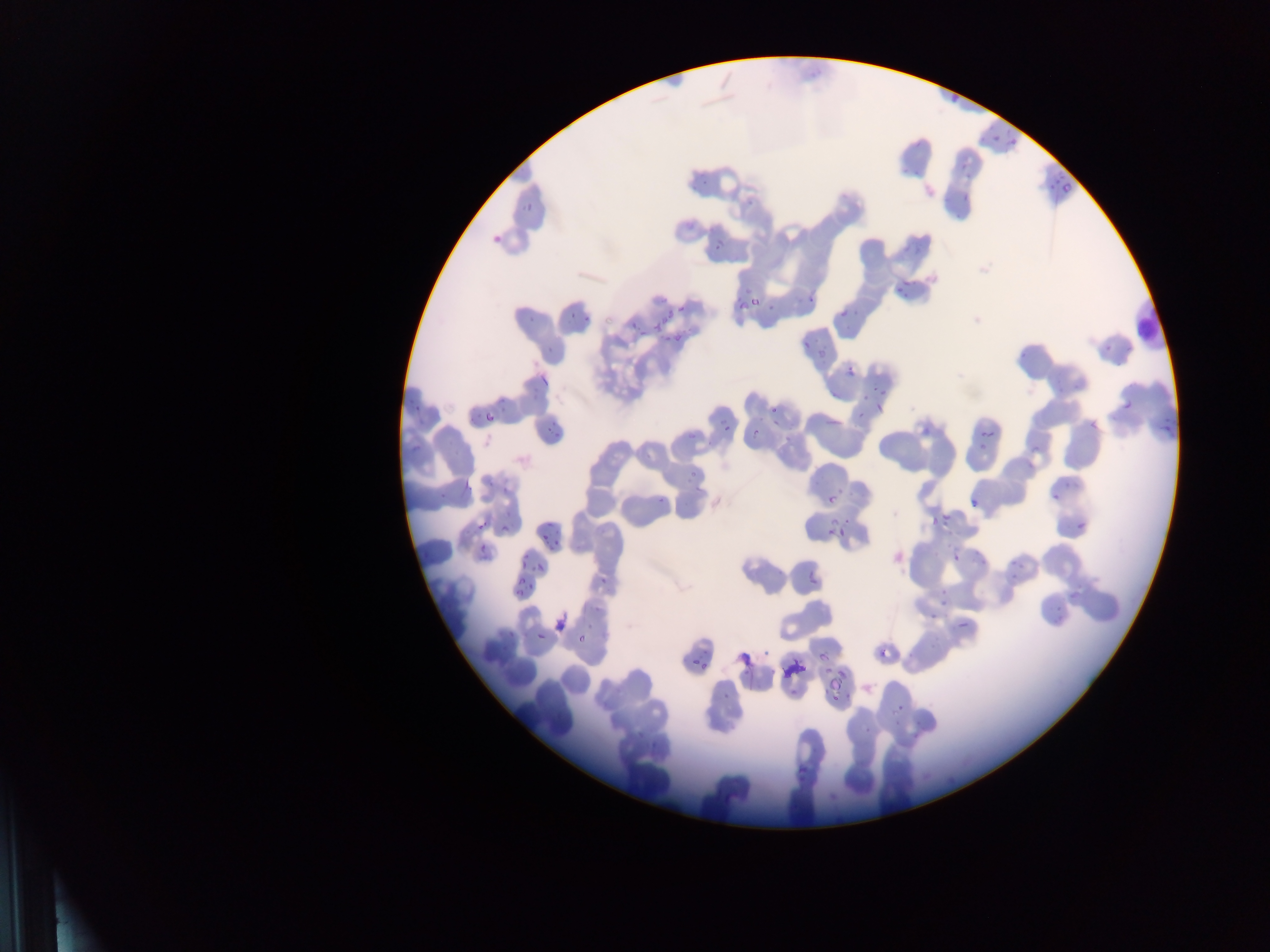
Approximate bounding boxes as (left, top, right, bottom) in pixels. Plasmodium parasite locations: (948, 94, 968, 104), (989, 127, 1005, 144), (1008, 137, 1018, 151), (958, 161, 971, 171), (1056, 173, 1076, 194), (1042, 176, 1056, 198), (523, 194, 544, 213), (958, 194, 969, 204), (485, 224, 503, 242), (708, 240, 727, 254), (892, 272, 917, 298), (736, 287, 764, 315), (802, 291, 816, 305), (835, 306, 848, 317), (523, 307, 541, 321), (568, 307, 600, 328), (625, 317, 644, 333), (656, 318, 675, 336), (545, 336, 562, 358), (1096, 336, 1114, 355), (799, 337, 815, 353), (843, 366, 859, 381), (533, 374, 549, 388), (870, 384, 891, 396), (856, 390, 872, 411), (1119, 396, 1139, 420), (764, 404, 778, 423), (479, 405, 496, 431), (875, 405, 885, 421), (542, 414, 564, 438), (921, 414, 939, 438), (1084, 414, 1104, 438), (720, 421, 727, 432), (1154, 421, 1176, 434), (688, 423, 706, 444), (976, 428, 997, 454), (748, 434, 758, 447), (687, 468, 701, 486), (459, 476, 477, 491), (1042, 488, 1065, 507), (822, 492, 840, 510), (655, 496, 668, 506), (965, 496, 980, 506), (933, 505, 960, 534), (822, 516, 844, 547), (499, 517, 510, 537), (1069, 517, 1090, 542), (474, 519, 489, 534), (540, 528, 551, 541), (548, 531, 566, 549), (475, 543, 486, 560), (888, 546, 911, 572), (516, 551, 532, 563), (950, 551, 965, 566), (1008, 554, 1028, 575), (532, 561, 546, 580), (803, 569, 814, 589), (599, 577, 610, 591), (515, 578, 529, 593), (925, 605, 944, 625), (554, 615, 563, 633), (953, 615, 976, 637), (535, 630, 549, 644), (575, 632, 587, 646), (875, 643, 895, 666), (815, 649, 832, 667), (737, 651, 755, 670), (691, 652, 701, 665), (700, 663, 713, 671), (832, 666, 851, 686), (824, 678, 840, 698), (889, 693, 910, 717), (860, 718, 875, 736), (794, 755, 812, 776). Leukocyte locations: (1134, 305, 1163, 346). Thin blood film. Image is 1270×952 pixels. Mobile-phone photograph taken through the microscope. Sample from Ghana. One field of view.